Locate every malaria parasite.
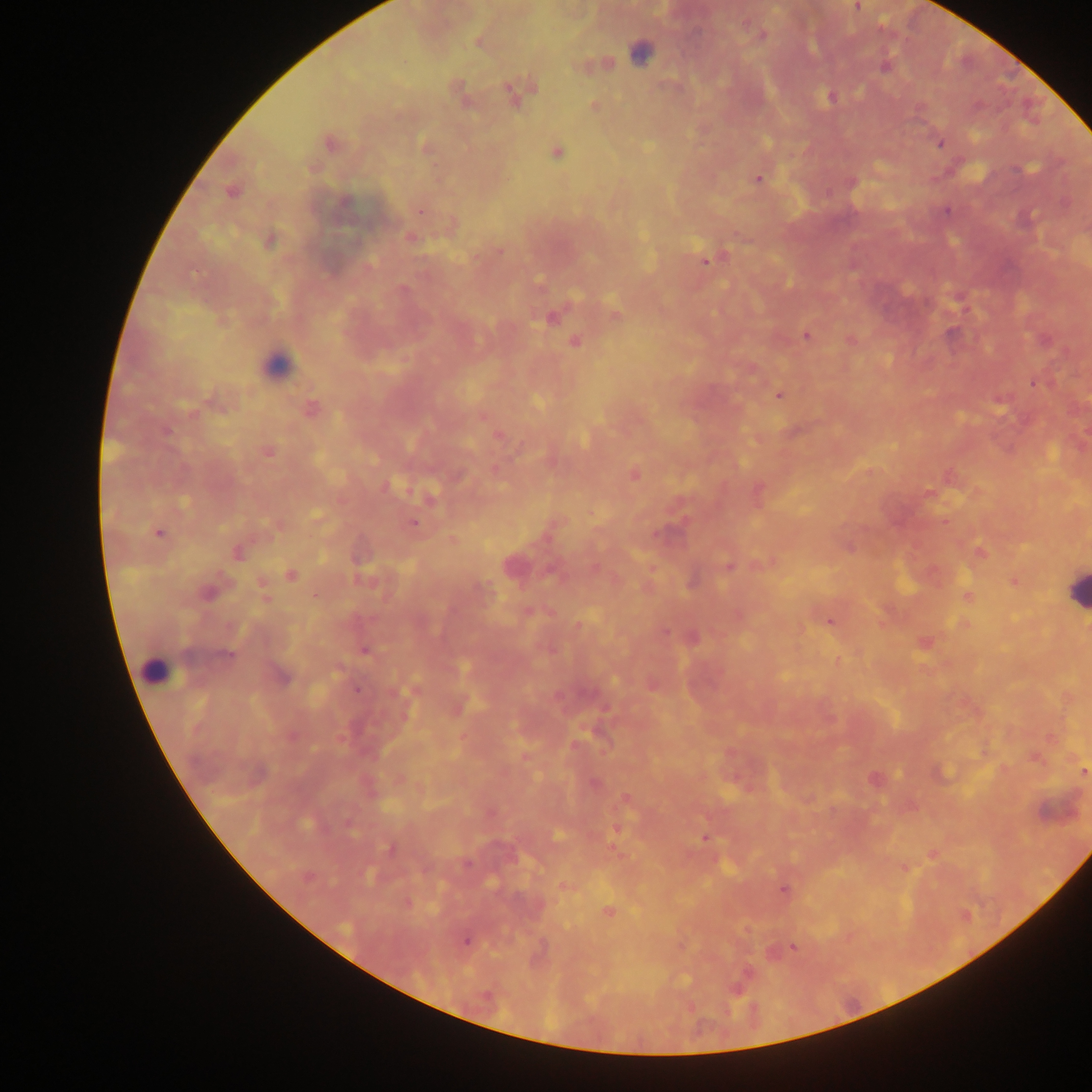

Approximate centers as [x, y] in pixels.
Malaria parasites: [857, 7], [761, 34], [477, 41], [640, 51], [606, 63], [885, 66], [517, 91], [462, 97], [830, 97], [593, 106], [329, 142], [940, 142], [426, 147], [556, 152], [757, 179], [231, 191], [344, 202], [420, 209], [409, 237], [270, 241], [499, 251], [705, 260], [615, 315], [551, 317], [807, 334], [851, 340], [574, 341], [1033, 382], [779, 395], [1000, 399], [214, 403], [310, 408], [498, 436], [267, 451], [496, 470], [633, 473], [758, 492], [928, 493], [430, 497], [413, 522], [277, 524], [158, 533], [452, 539], [238, 552], [980, 552], [769, 563], [512, 566], [728, 566], [290, 575], [364, 579], [1014, 580], [207, 591], [264, 592], [967, 595], [530, 612], [738, 615], [828, 621], [965, 624], [578, 625], [691, 638], [924, 642], [364, 650], [837, 661], [280, 675], [652, 684], [413, 689], [457, 707], [1049, 736], [575, 746], [526, 756], [1034, 756], [1083, 772], [874, 779], [593, 783], [625, 798], [616, 828], [704, 837], [391, 848], [932, 854], [904, 867], [307, 877], [564, 885], [783, 889], [608, 911], [465, 939], [792, 946], [746, 973].

Summary:
  - Leukocyte locations: [275, 365], [1077, 592], [154, 672]
  - Preparation: thick blood film
  - Image size: 1092×1092 pixels
  - Field of view: single
  - Capture: mobile-phone photograph through a microscope
  - Country: Ghana